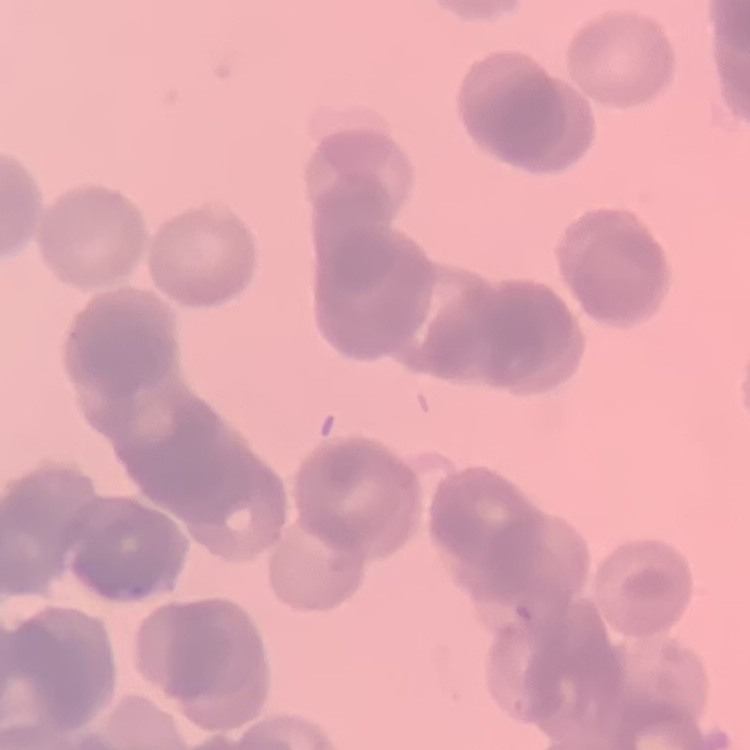 The red blood cells exhibit rouleaux formation. Thin blood smear. Field's or Giemsa stain. Square crop of a larger photomicrograph.